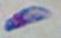

modality = photomicrograph
identification = Toxoplasma gondii
magnification = 1000x